Name the parasite shown.
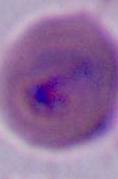

This is Plasmodium.

Captured at either 400x or 1000x magnification. Photomicrograph.